Identify the parasite.
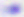

This is Toxoplasma gondii.

magnification = 400x
modality = photomicrograph